Classify this cell by malaria status.
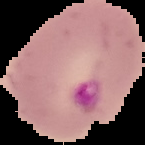
It is parasitized.

Summary:
  - Image size: 145×145 pixels
  - Image type: segmented cell region with the area outside set to black
  - Preparation: thin blood smear